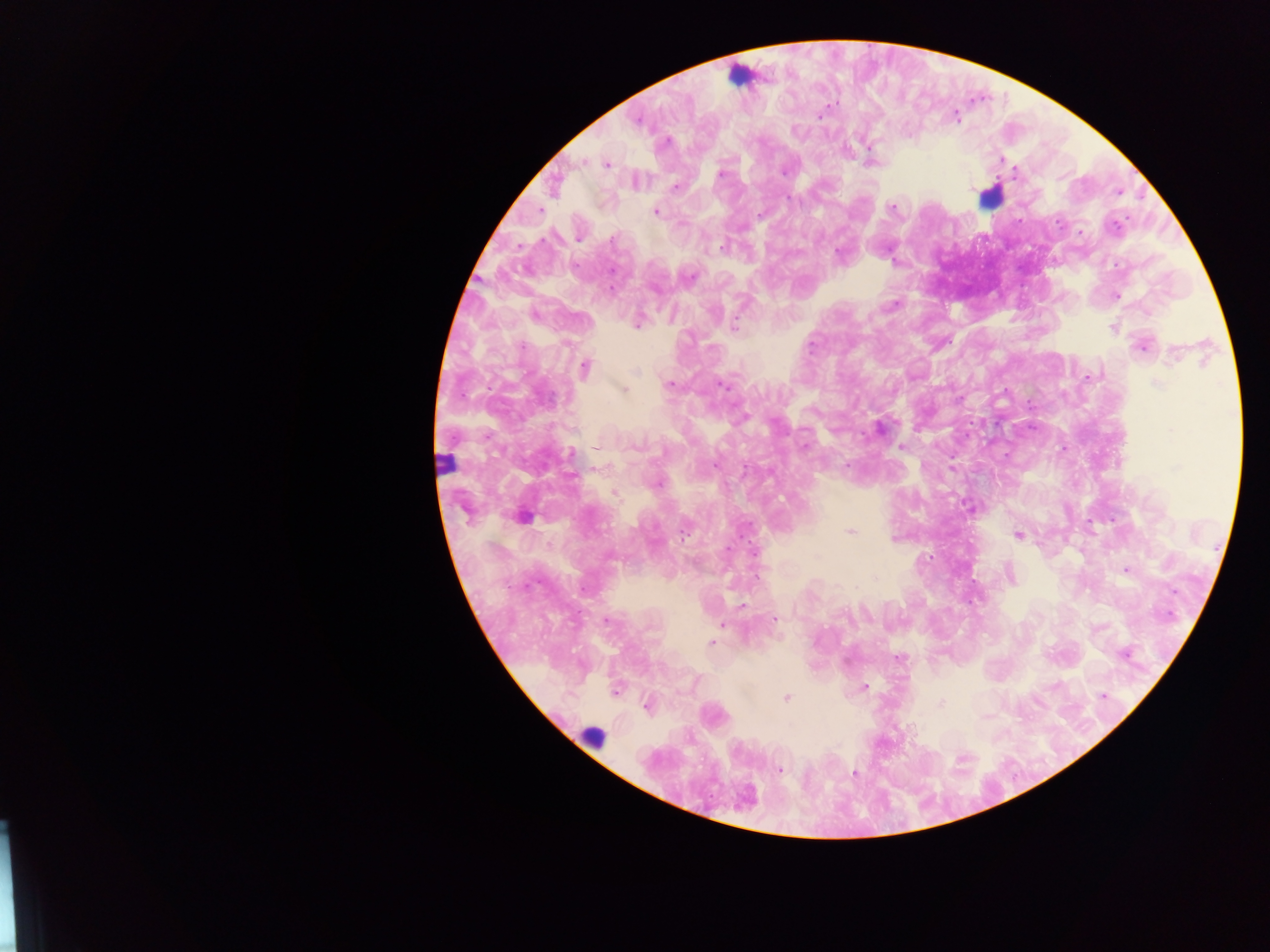
Approximate centers as [x, y] in pixels. Leukocyte locations: [739, 75], [989, 197], [448, 464], [592, 737]. Plasmodium parasite locations: [821, 115], [956, 117], [637, 120], [667, 141], [869, 145], [1003, 159], [581, 162], [606, 164], [1014, 170], [783, 172], [721, 174], [676, 188], [790, 198], [893, 207], [656, 212], [760, 214], [1116, 225], [1080, 232], [578, 238], [613, 239], [722, 246], [838, 253], [690, 277], [612, 286], [1116, 296], [893, 304], [535, 315], [638, 323], [734, 325], [1112, 327], [523, 346], [1141, 346], [1174, 355], [585, 368], [637, 372], [1088, 377], [669, 384], [1157, 384], [722, 385], [623, 389], [880, 427], [806, 445], [635, 446], [902, 447], [599, 448], [571, 454], [715, 465], [847, 465], [744, 470], [657, 484], [614, 493], [850, 531], [684, 533], [1018, 536], [893, 539], [728, 549], [1126, 571], [1011, 575], [876, 577], [584, 589], [742, 605], [606, 620], [774, 620], [722, 625], [711, 643], [1124, 655], [898, 658], [864, 686], [615, 691], [1102, 696], [786, 698], [941, 704], [646, 706], [779, 769], [854, 774]. Collected in Ghana. Image is 1270×952 pixels. Thick blood smear. Mobile-phone photograph taken through the microscope. One field of view.